Name the parasite shown.
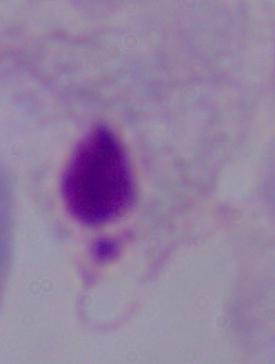

This is a trichomonad.

Summary:
  - Modality: photomicrograph
  - Magnification: 1000x